Outline each blood parasite and name the species.
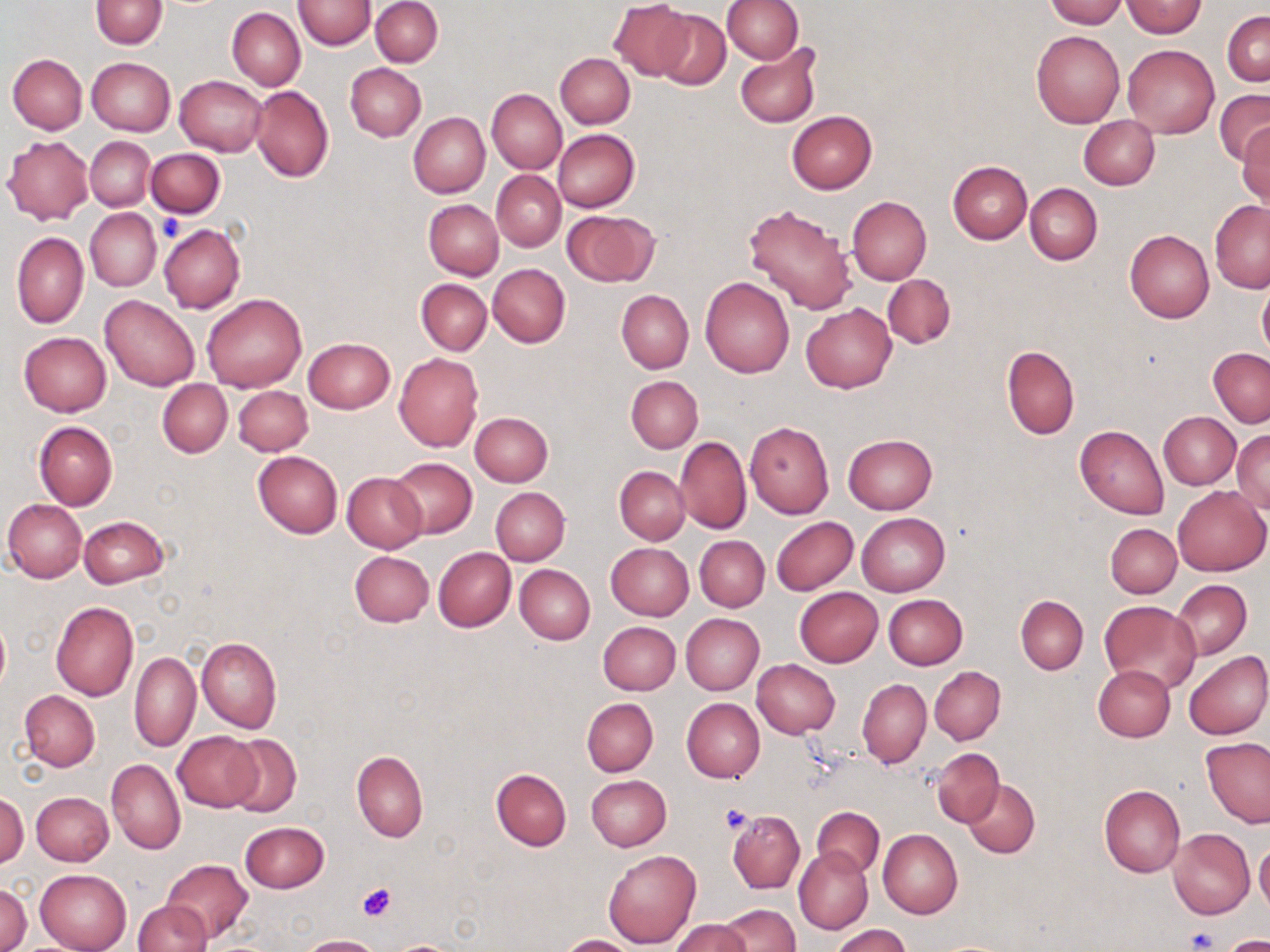

No blood parasites observed.

Approximate bounding boxes as [x1, y1, x2, y2] in pixels. Uninfected red blood cell locations: [91, 0, 167, 49], [292, 0, 376, 49], [371, 0, 443, 67], [722, 0, 803, 63], [1044, 0, 1125, 27], [609, 1, 694, 80], [1124, 2, 1205, 36], [226, 7, 305, 90], [654, 10, 731, 89], [1222, 12, 1270, 86], [1032, 30, 1124, 127], [1122, 44, 1219, 138], [735, 47, 822, 127], [554, 52, 635, 128], [8, 54, 87, 134], [87, 57, 174, 137], [345, 63, 425, 141], [175, 76, 268, 156], [249, 84, 334, 182], [487, 88, 566, 174], [1214, 89, 1270, 167], [786, 111, 877, 194], [408, 112, 489, 197], [1079, 116, 1160, 190], [1236, 124, 1270, 210], [552, 129, 640, 212], [86, 135, 155, 211], [3, 136, 94, 224], [145, 148, 226, 218], [947, 160, 1032, 243], [492, 171, 566, 251], [1024, 183, 1102, 264], [847, 196, 932, 284], [424, 199, 503, 280], [1210, 200, 1270, 292], [742, 204, 857, 314], [85, 208, 160, 290], [562, 209, 657, 287], [159, 224, 245, 314], [1124, 230, 1213, 322], [12, 233, 89, 328], [487, 264, 570, 348], [883, 275, 955, 348], [700, 277, 795, 378], [416, 278, 491, 354], [1258, 278, 1270, 362], [617, 290, 693, 373], [101, 294, 201, 391], [202, 295, 305, 392], [801, 304, 896, 393], [19, 332, 111, 416], [303, 338, 395, 413], [1002, 345, 1079, 439], [1208, 348, 1270, 428], [394, 353, 484, 453], [625, 376, 702, 453], [157, 379, 232, 457], [233, 384, 313, 455], [470, 411, 553, 487], [1158, 411, 1241, 489], [482, 413, 560, 563], [34, 421, 117, 510], [743, 421, 835, 518], [1075, 425, 1168, 518], [1232, 430, 1270, 514], [843, 434, 937, 514], [674, 436, 750, 534], [253, 451, 343, 538], [389, 456, 477, 538], [614, 465, 690, 544], [342, 472, 427, 554], [1172, 485, 1269, 576], [490, 488, 569, 566], [3, 499, 87, 582], [857, 513, 950, 596], [79, 516, 167, 589], [771, 516, 857, 595], [1106, 524, 1181, 597], [695, 536, 769, 612], [606, 543, 694, 620], [433, 547, 516, 632], [350, 551, 433, 627], [515, 563, 595, 643], [1174, 579, 1252, 659], [793, 587, 883, 667], [883, 594, 967, 669], [1016, 595, 1088, 674], [1099, 600, 1202, 695], [51, 601, 139, 701], [681, 614, 764, 694], [0, 615, 10, 695], [598, 621, 680, 695], [197, 637, 282, 733], [1184, 651, 1270, 740], [130, 652, 200, 752], [752, 660, 839, 738], [1093, 665, 1176, 741], [930, 667, 1005, 744], [858, 678, 931, 769], [20, 690, 99, 771], [582, 698, 658, 776], [681, 698, 765, 783], [172, 731, 260, 811], [224, 733, 302, 818], [1200, 737, 1270, 828], [931, 748, 1004, 827], [352, 750, 428, 841], [107, 758, 185, 855], [491, 768, 571, 851], [586, 776, 671, 851], [963, 780, 1039, 858], [1099, 783, 1184, 877], [31, 791, 113, 865], [1, 793, 27, 870], [812, 806, 884, 877], [727, 810, 805, 894], [239, 821, 328, 893], [877, 829, 962, 918], [1168, 829, 1254, 920], [1255, 840, 1270, 916], [794, 848, 873, 935], [603, 850, 701, 949], [162, 860, 252, 942], [34, 870, 131, 952], [0, 882, 31, 952], [132, 900, 210, 952], [717, 904, 800, 952], [672, 919, 751, 952], [831, 925, 910, 952], [299, 934, 383, 952], [557, 934, 642, 952], [1218, 935, 1270, 952], [385, 938, 469, 951]. Platelet locations: [157, 213, 185, 242], [720, 806, 753, 835], [357, 883, 395, 920], [1187, 927, 1217, 951]. Slide-level diagnosis: no evidence of blood parasites. Image is 1270×952 pixels. 1000x magnification. Optical microscopy. Thin blood film. Single field of view. May-Grünwald-Giemsa stain.